Identify the cell.
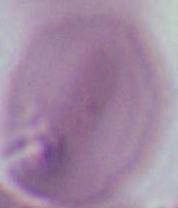
This is an erythrocyte.

Summary:
  - Modality: micrograph
  - Magnification: 1000x